State the preparation type.
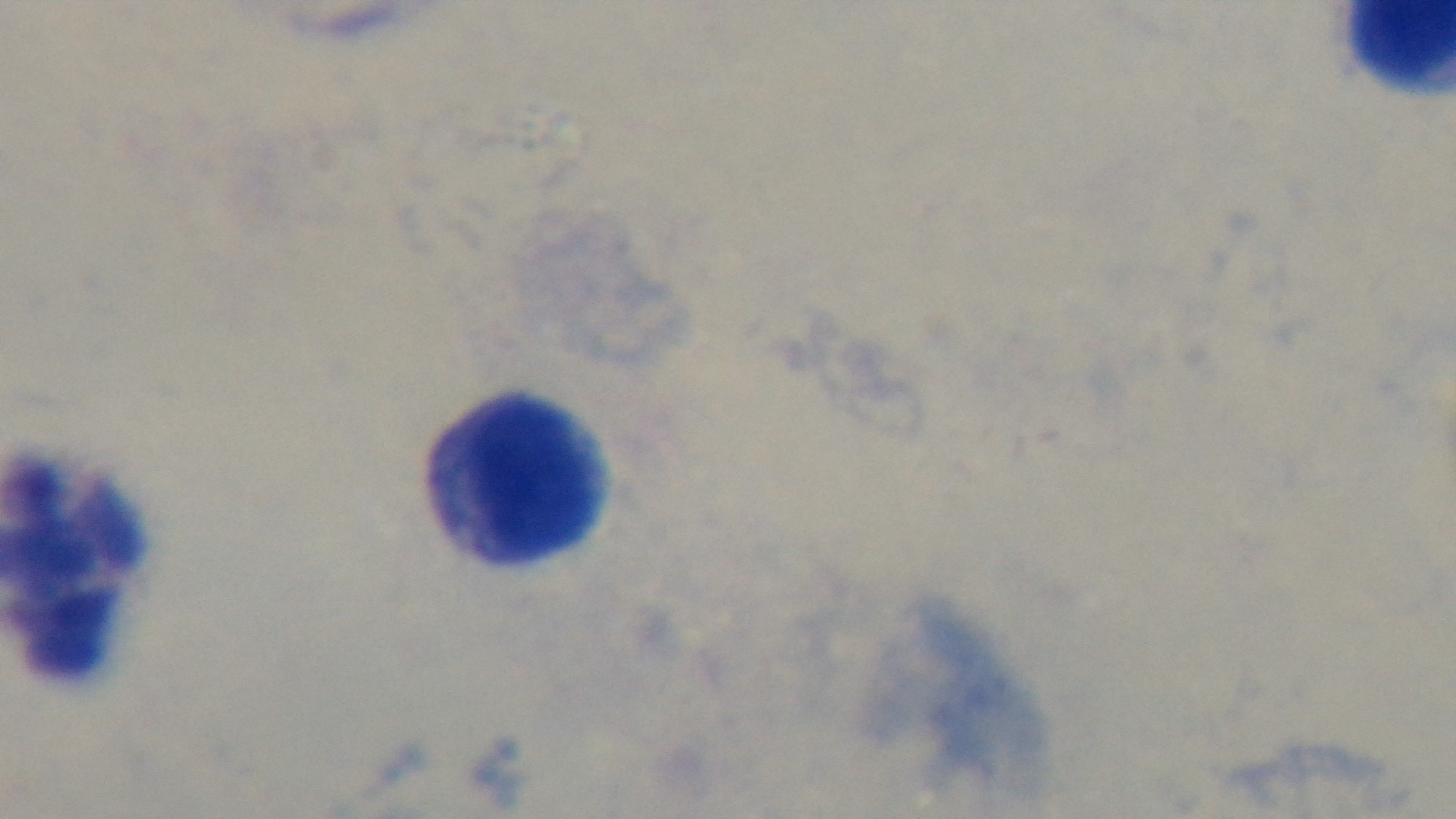

It is a thick blood film.

Oil-immersion objective, 100x. Giemsa-stained. Captured with a mounted 4K digital camera. Malaria status: uninfected. Single field of view. Photomicrograph.